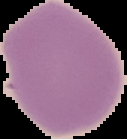 Result: negative for malaria parasites. Segmented cell region on a black background. From a thin blood smear. Image is 127×139 pixels.